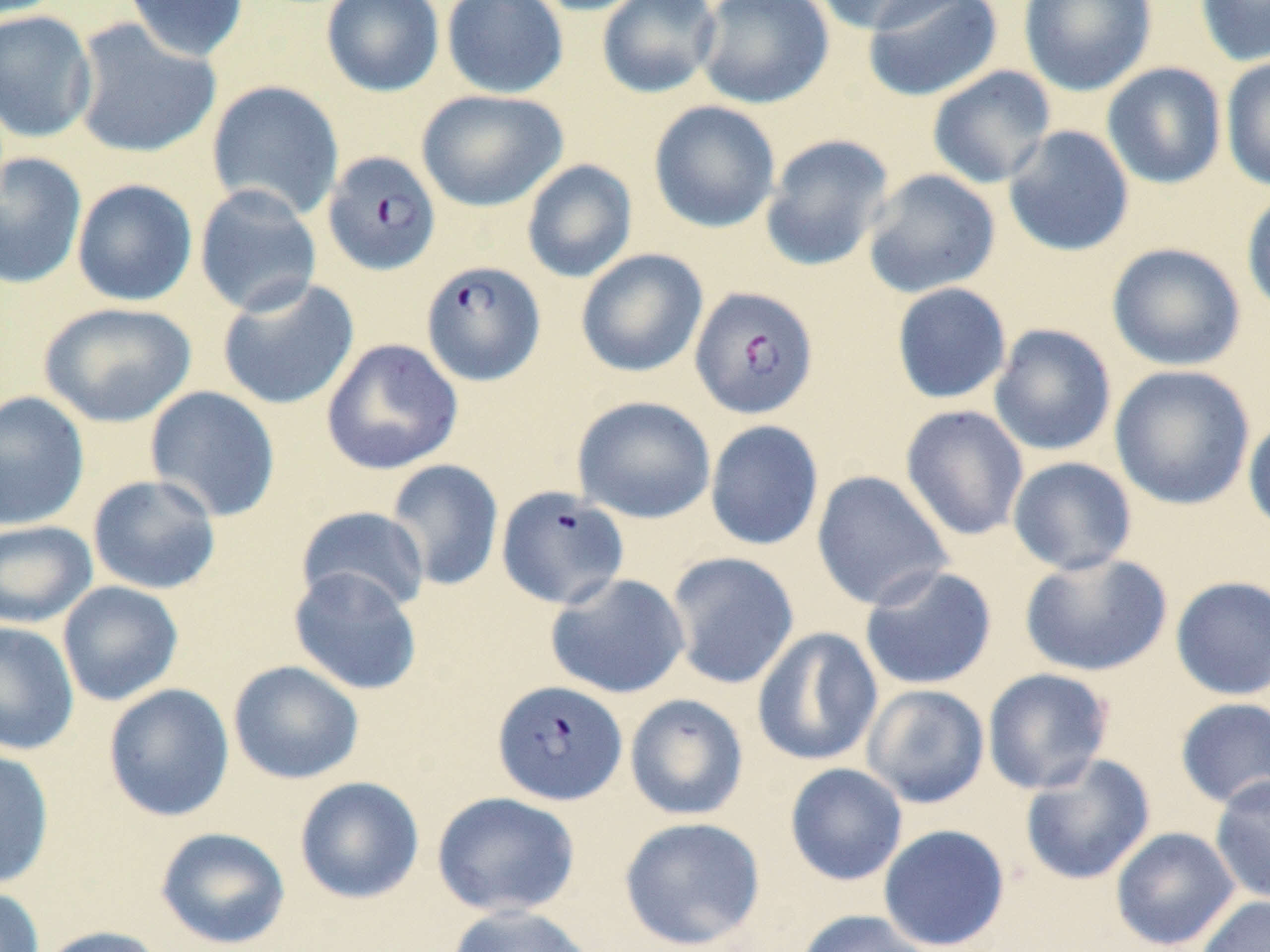
slide-level diagnosis = Plasmodium falciparum
magnification = 1000x
uninfected red blood cell locations = approximate bounding boxes as (x1,y1)-(x2,y2) corner pairs in pixels: (121,0)-(250,61), (321,0)-(445,97), (441,0)-(569,99), (525,0)-(655,16), (596,0)-(722,99), (695,0)-(834,108), (810,0)-(963,36), (1018,0)-(1157,96), (1194,0)-(1270,67), (862,1)-(1004,102), (0,10)-(97,143), (70,18)-(221,159), (1221,55)-(1270,192), (1102,62)-(1227,189), (927,66)-(1057,189), (207,80)-(344,221), (416,89)-(568,212), (648,100)-(781,233), (1003,125)-(1135,257), (760,134)-(895,272), (0,152)-(88,290), (521,159)-(638,283), (862,168)-(1000,299), (71,178)-(198,307), (193,184)-(323,318), (1241,188)-(1270,318), (1106,242)-(1246,371), (575,249)-(708,378), (216,277)-(360,411), (890,283)-(1012,405), (38,301)-(197,427), (988,324)-(1117,457), (321,338)-(464,476), (1109,365)-(1256,510), (144,386)-(281,522), (0,391)-(90,531), (572,395)-(716,524), (900,404)-(1029,541), (1243,413)-(1270,537), (705,420)-(824,551), (1007,457)-(1137,576), (384,459)-(504,592), (811,470)-(953,611), (87,474)-(222,595), (295,506)-(431,614), (0,520)-(98,629), (666,551)-(800,689), (1018,552)-(1173,678), (859,565)-(998,690), (288,566)-(424,696), (545,572)-(690,699), (1170,576)-(1270,700), (57,581)-(184,706), (0,621)-(80,755), (751,627)-(883,767), (227,660)-(364,785), (982,668)-(1114,794), (103,683)-(235,822), (861,684)-(990,809), (624,693)-(749,821), (1175,698)-(1270,811), (0,748)-(55,890), (1019,754)-(1156,886), (784,763)-(908,886), (1209,775)-(1270,905), (294,776)-(425,904), (431,791)-(581,918), (619,816)-(766,951), (877,824)-(1010,951), (155,826)-(291,950), (1109,827)-(1242,951), (0,886)-(45,952), (1194,894)-(1270,952), (445,904)-(598,952), (793,909)-(934,952), (36,925)-(167,952)
image size = 1270×952 pixels
preparation = thin blood smear
modality = light microscopy
field of view = single
Plasmodium falciparum-infected red blood cell locations = approximate bounding boxes as (x1,y1)-(x2,y2) corner pairs in pixels: (322,151)-(441,276), (420,260)-(545,386), (690,285)-(820,420), (496,486)-(630,610), (492,679)-(627,806)
stain = May-Grünwald-Giemsa